Comment on the morphology of the red blood cells.
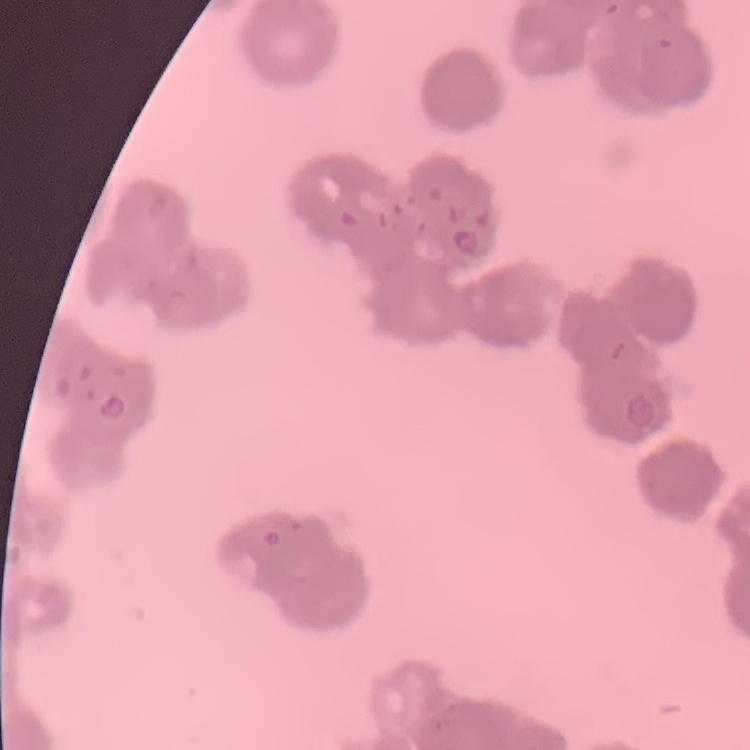
Rouleaux formation.

Thin blood smear. Field's or Giemsa stain. One tile cut from a larger photomicrograph.